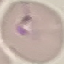
result = no malaria parasites seen
image type = automatically extracted cell patch, resized to 64 × 64 pixels
stain = Giemsa
preparation = thin smear
capture = smartphone camera at the microscope eyepiece